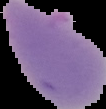

image_type: segmented cell region with the area outside set to black
result: no Plasmodium parasites detected
image_size: 106×109 pixels
preparation: thin blood smear